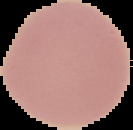

Summary:
  - Image type: segmented cell region with the area outside set to black
  - Image size: 133×130 pixels
  - Malaria status: uninfected
  - Preparation: thin blood film